Give the position of every Plasmodium parasite.
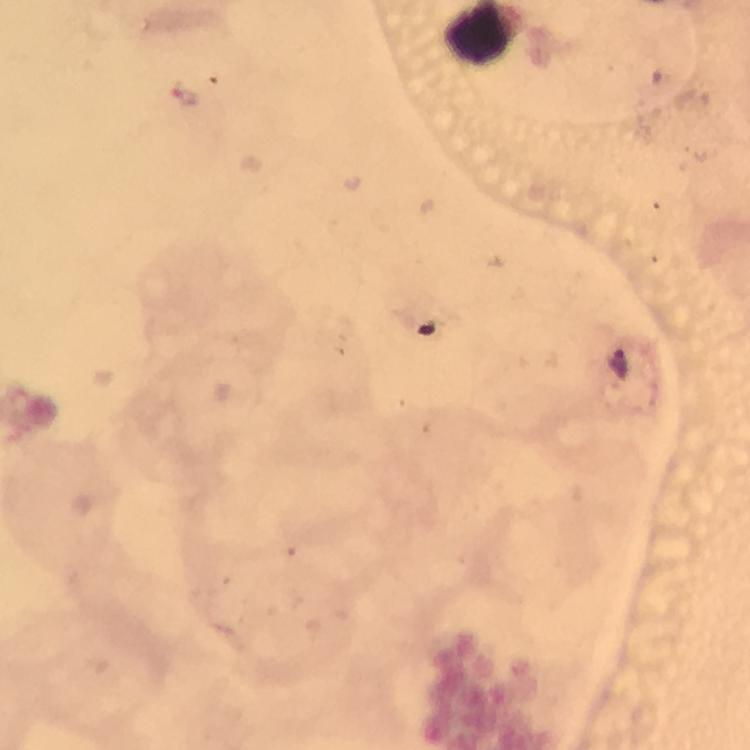

Approximate centers as [x, y] in pixels.
Plasmodium parasites: [186, 97], [618, 364].

context = from a malaria diagnostic workup
cropped from = one field of view
stain = Giemsa
magnification = 100x
image size = 750×750 pixels
capture = smartphone camera through the microscope
preparation = thick blood film
immersion oil = used